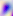
Summary:
  - Modality: photomicrograph
  - Identification: Toxoplasma gondii
  - Magnification: 400x